Look for Plasmodium parasites.
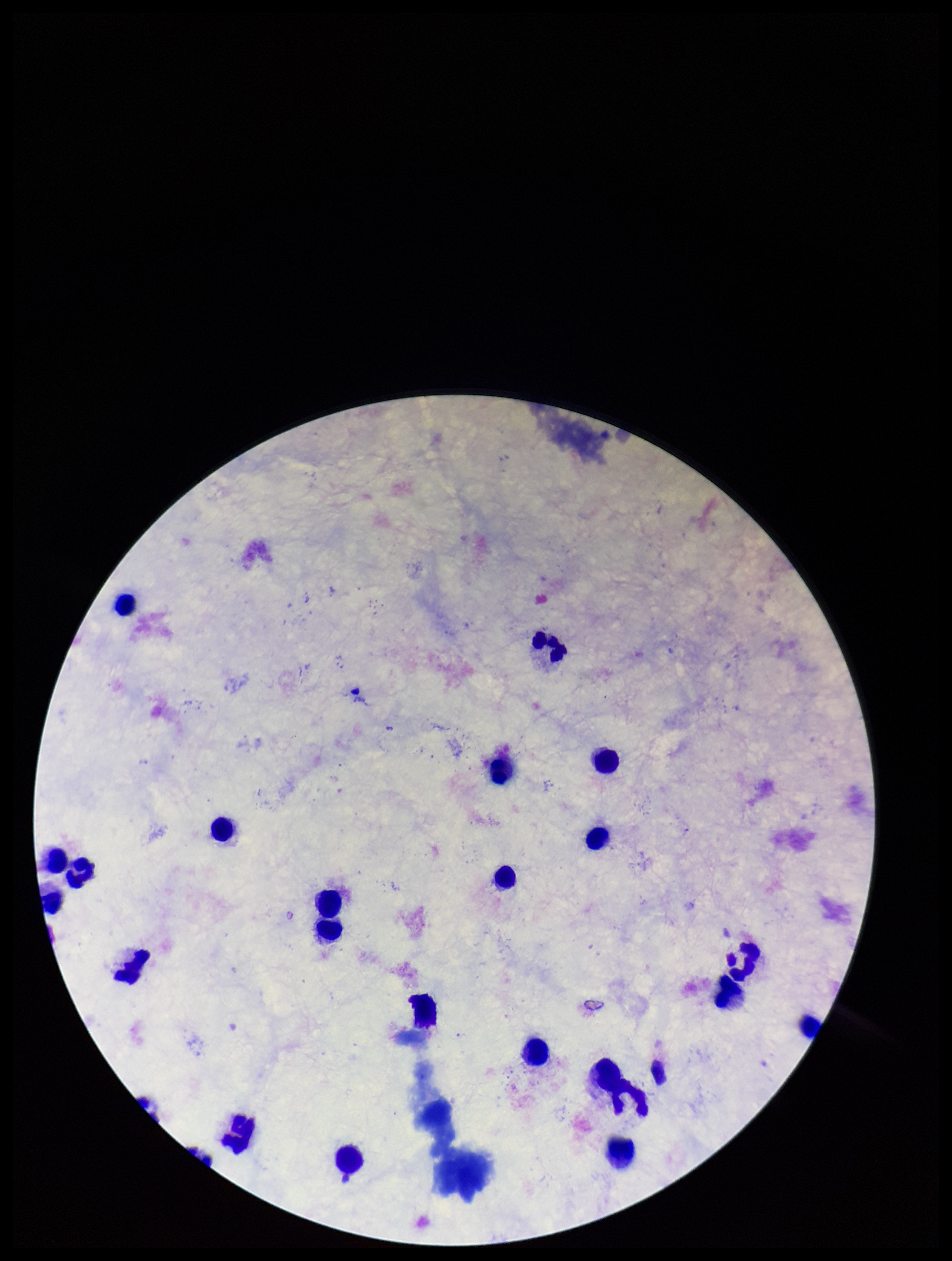
None seen.

Summary:
  - Parasite count: 0
  - Leukocyte count: 23
  - Preparation: thick blood smear
  - Image size: 952×1261 pixels
  - Field of view: single
  - Capture: smartphone photograph through the microscope eyepiece
  - Stain: Giemsa
  - Patient malaria status: negative